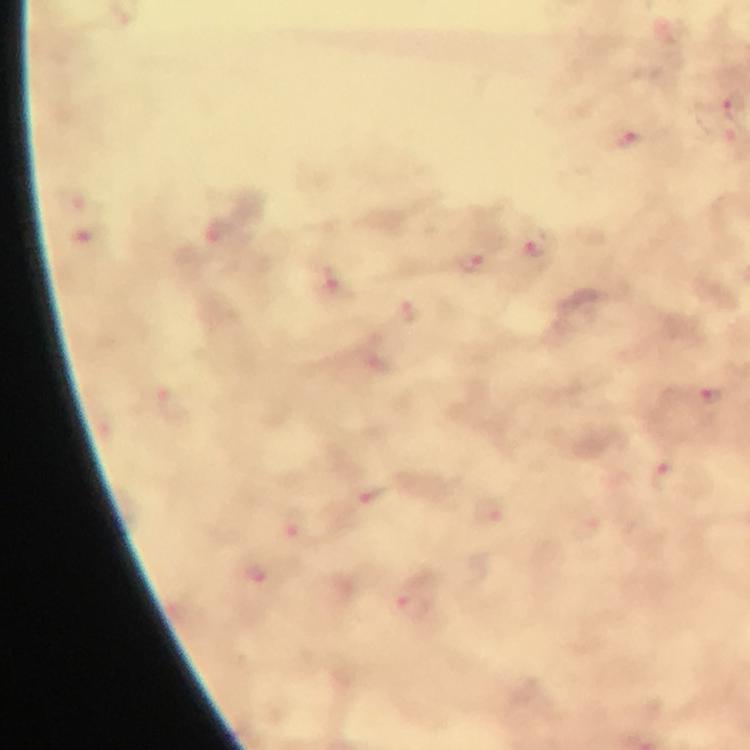
Approximate centers as {x, y} in pixels.
Summary:
  - Malaria parasite locations: {733, 106}, {627, 140}, {539, 249}, {472, 262}, {333, 284}, {409, 312}, {709, 396}, {373, 497}, {255, 573}, {411, 606}
  - Image size: 750×750 pixels
  - Immersion oil: applied
  - Stain: Giemsa
  - Preparation: thick blood film
  - Cropped from: one field of view
  - Capture: smartphone camera through the microscope
  - Magnification: 100x
  - Context: from a diagnostic examination for malaria